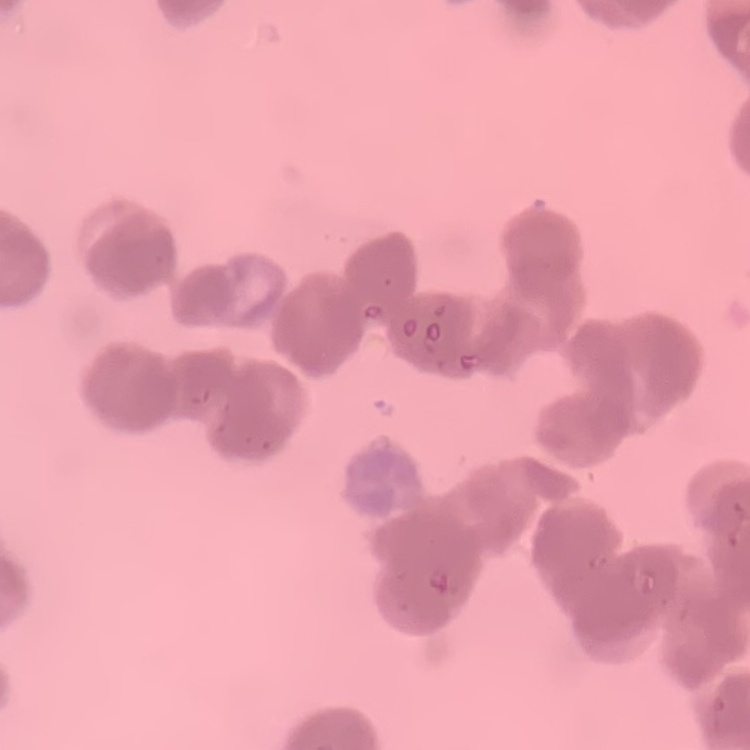

erythrocyte morphology = rouleaux formation
image type = one tile cut from a larger photomicrograph
preparation = thin blood film
stain = Field's or Giemsa